Assess the morphology of the red blood cells.
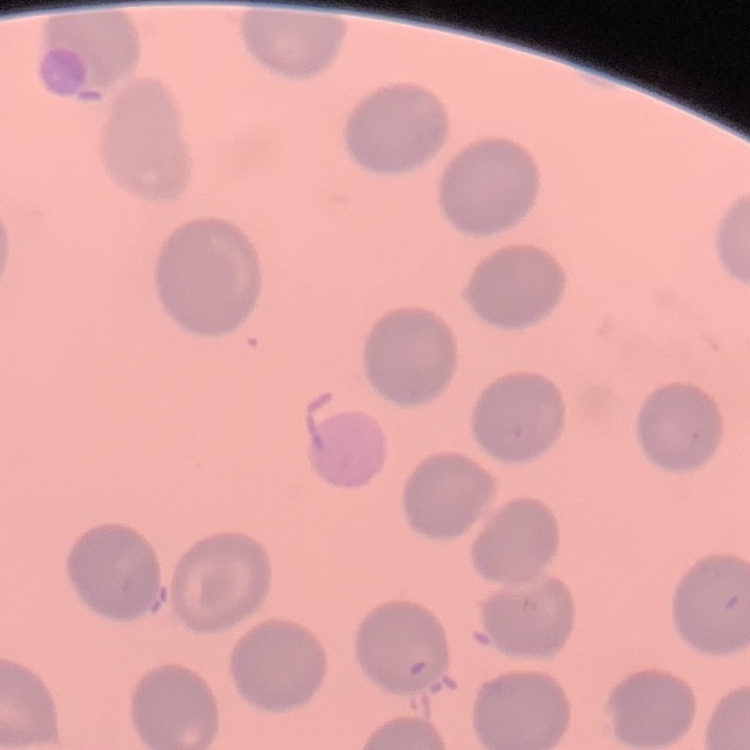
No rouleaux formation.

image type = square crop of a larger photomicrograph
preparation = thin peripheral smear
stain = Field's or Giemsa